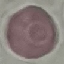

result = negative for malaria parasites
preparation = thin smear
image type = automatically extracted cell patch, resized to 64 × 64 pixels
stain = Giemsa
capture = smartphone camera at the microscope eyepiece